Locate and identify every blood parasite.
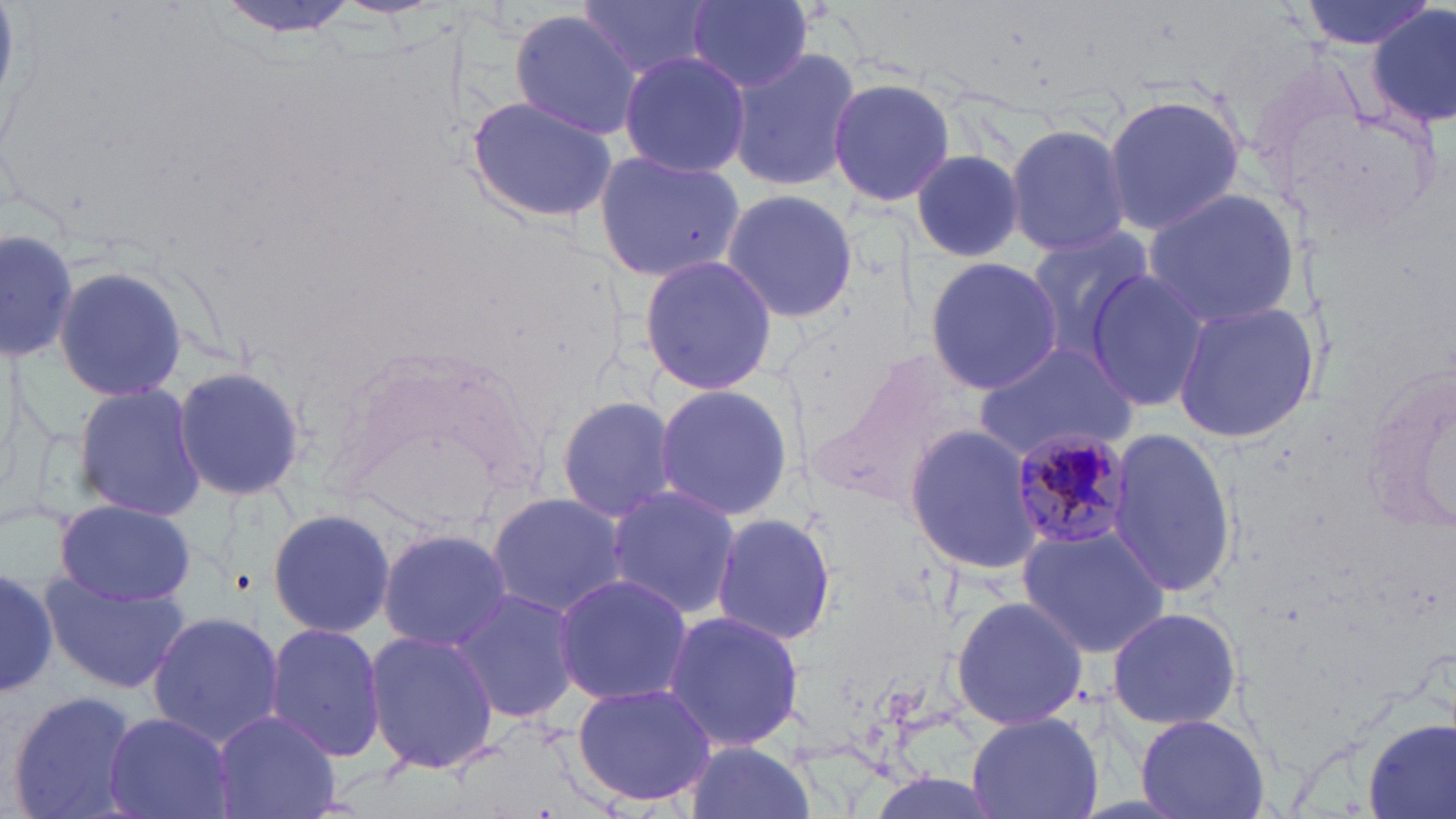

Approximate bounding boxes as named x1/y1/x2/y2 corners in pixels.
Plasmodium malariae-infected red blood cells: (x1=1010, y1=429, x2=1136, y2=551).
No Plasmodium falciparum, Plasmodium ovale, Plasmodium vivax, Babesia divergens, or Trypanosoma brucei observed.

slide-level diagnosis = Plasmodium malariae
field of view = single
uninfected red blood cell locations = approximate bounding boxes as named x1/y1/x2/y2 corners in pixels: (x1=214, y1=0, x2=366, y2=39), (x1=577, y1=0, x2=715, y2=81), (x1=1297, y1=0, x2=1435, y2=50), (x1=688, y1=1, x2=814, y2=93), (x1=1370, y1=5, x2=1455, y2=131), (x1=509, y1=8, x2=642, y2=139), (x1=728, y1=46, x2=862, y2=194), (x1=618, y1=49, x2=750, y2=176), (x1=827, y1=76, x2=956, y2=209), (x1=1101, y1=92, x2=1247, y2=235), (x1=465, y1=93, x2=619, y2=227), (x1=1004, y1=124, x2=1132, y2=255), (x1=911, y1=146, x2=1030, y2=263), (x1=593, y1=149, x2=744, y2=284), (x1=1141, y1=187, x2=1300, y2=326), (x1=720, y1=188, x2=860, y2=323), (x1=0, y1=224, x2=79, y2=359), (x1=1017, y1=225, x2=1156, y2=366), (x1=637, y1=253, x2=777, y2=396), (x1=923, y1=257, x2=1063, y2=395), (x1=51, y1=264, x2=188, y2=403), (x1=1083, y1=267, x2=1211, y2=415), (x1=1168, y1=299, x2=1322, y2=444), (x1=971, y1=341, x2=1137, y2=461), (x1=174, y1=361, x2=308, y2=503), (x1=72, y1=382, x2=207, y2=520), (x1=650, y1=382, x2=795, y2=524), (x1=556, y1=394, x2=681, y2=523), (x1=904, y1=423, x2=1042, y2=576), (x1=1106, y1=425, x2=1238, y2=597), (x1=605, y1=485, x2=740, y2=618), (x1=484, y1=492, x2=630, y2=616), (x1=53, y1=502, x2=197, y2=606), (x1=265, y1=505, x2=396, y2=640), (x1=709, y1=510, x2=838, y2=649), (x1=1014, y1=526, x2=1172, y2=657), (x1=377, y1=529, x2=515, y2=650), (x1=0, y1=564, x2=59, y2=697), (x1=39, y1=570, x2=191, y2=694), (x1=552, y1=573, x2=696, y2=706), (x1=449, y1=588, x2=583, y2=724), (x1=950, y1=594, x2=1089, y2=729), (x1=1104, y1=604, x2=1244, y2=733), (x1=659, y1=609, x2=806, y2=753), (x1=147, y1=610, x2=286, y2=748), (x1=263, y1=622, x2=385, y2=763), (x1=365, y1=630, x2=498, y2=776), (x1=570, y1=681, x2=716, y2=810), (x1=5, y1=688, x2=143, y2=819), (x1=102, y1=711, x2=236, y2=819), (x1=210, y1=711, x2=342, y2=819), (x1=965, y1=712, x2=1103, y2=819), (x1=1135, y1=714, x2=1270, y2=819), (x1=1364, y1=715, x2=1456, y2=819), (x1=680, y1=739, x2=818, y2=819)
modality = optical microscopy
magnification = 1000x
stain = May-Grünwald-Giemsa
image size = 1456×819 pixels
preparation = thin blood film